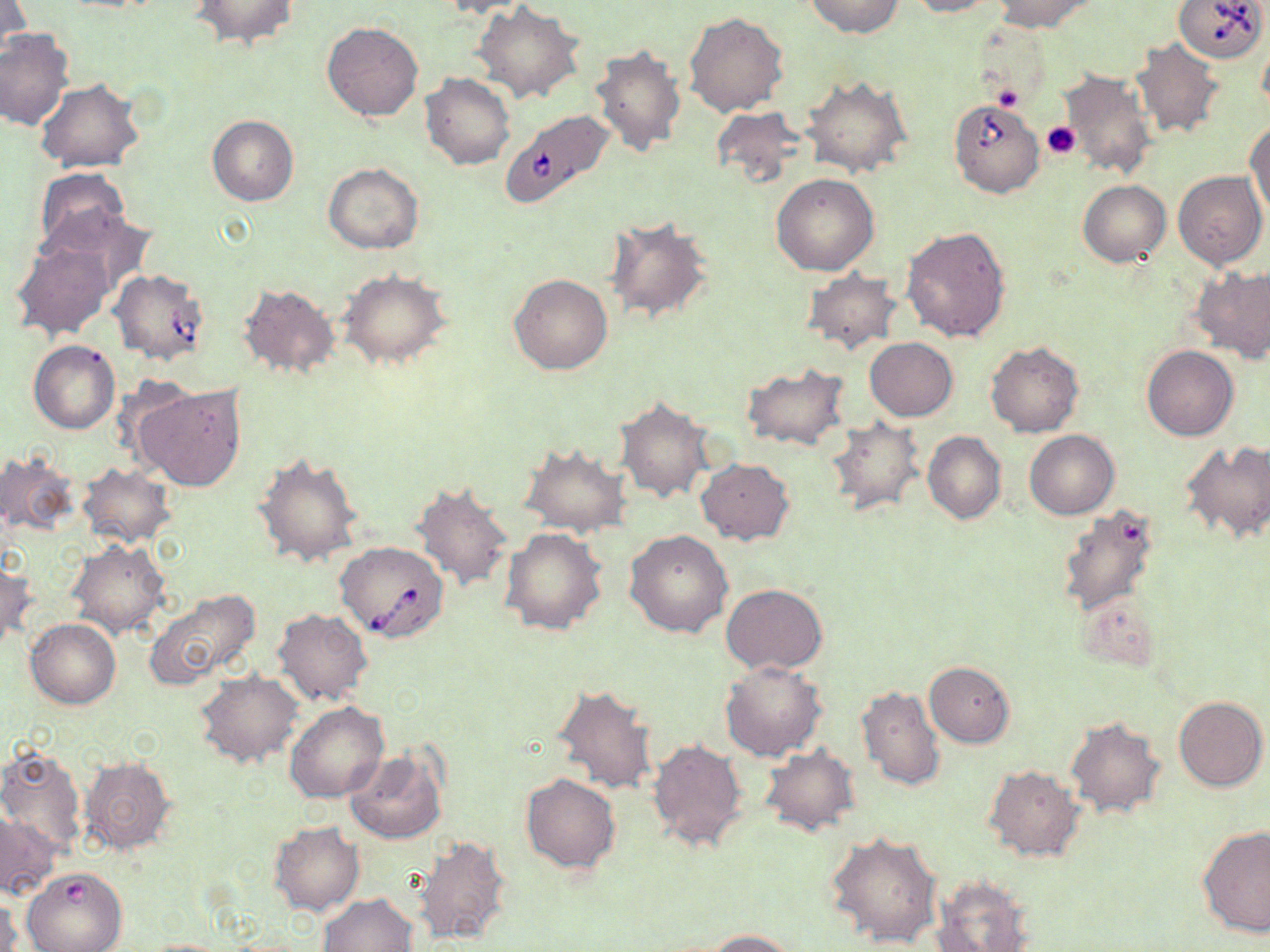
Approximate bounding boxes as (x1, y1, x2, y2) in pixels. Babesia divergens-infected red blood cell locations: (1174, 0, 1268, 63), (948, 98, 1044, 197), (502, 111, 614, 209), (107, 268, 211, 364), (335, 541, 448, 642). Uninfected red blood cell locations: (0, 0, 28, 64), (433, 0, 532, 18), (805, 0, 903, 38), (905, 0, 996, 18), (992, 0, 1096, 33), (191, 1, 299, 48), (472, 3, 585, 102), (684, 10, 789, 116), (321, 20, 424, 121), (0, 28, 75, 130), (1257, 37, 1269, 117), (1131, 39, 1225, 139), (592, 44, 687, 156), (1057, 68, 1157, 179), (421, 73, 516, 170), (802, 75, 912, 179), (34, 79, 143, 172), (711, 105, 810, 189), (207, 115, 299, 206), (1246, 121, 1269, 217), (324, 163, 424, 253), (34, 168, 132, 256), (1173, 172, 1266, 268), (771, 173, 880, 276), (1078, 180, 1170, 266), (44, 207, 153, 296), (603, 215, 715, 324), (900, 224, 1012, 343), (11, 240, 114, 340), (1191, 267, 1270, 362), (800, 268, 903, 355), (337, 269, 454, 369), (508, 273, 613, 375), (237, 282, 341, 380), (864, 337, 957, 420), (29, 340, 120, 434), (986, 341, 1085, 438), (1141, 345, 1239, 441), (741, 364, 850, 452), (134, 382, 247, 492), (615, 396, 714, 503), (824, 416, 926, 518), (1024, 430, 1118, 519), (924, 431, 1005, 525), (1181, 441, 1270, 544), (519, 443, 631, 536), (0, 448, 79, 536), (252, 451, 364, 567), (696, 458, 795, 544), (77, 463, 176, 547), (410, 482, 514, 593), (1056, 503, 1162, 618), (500, 528, 607, 635), (624, 529, 732, 637), (67, 541, 171, 637), (1, 560, 35, 650), (722, 584, 826, 674), (143, 588, 262, 690), (272, 607, 374, 706), (26, 618, 121, 709), (719, 661, 826, 760), (924, 661, 1016, 747), (194, 670, 303, 768), (552, 683, 658, 795), (854, 684, 946, 790), (1173, 695, 1267, 791), (285, 701, 389, 803), (1065, 717, 1169, 820), (646, 738, 749, 851), (0, 745, 89, 857), (758, 745, 861, 836), (345, 748, 447, 843), (80, 757, 177, 855), (984, 765, 1084, 862), (520, 773, 621, 874), (0, 809, 58, 901), (270, 822, 362, 915), (1198, 825, 1270, 937), (825, 831, 943, 949), (415, 836, 512, 944), (21, 866, 128, 952), (933, 876, 1037, 952), (1, 893, 22, 952), (319, 893, 418, 952), (702, 929, 801, 951). Platelet locations: (992, 85, 1024, 113), (1043, 121, 1080, 159). Slide-level diagnosis: Babesia divergens. Single field of view. Image is 1270×952 pixels. Thin blood film. Light microscopy. May-Grünwald-Giemsa-stained preparation. Captured at 1000x magnification.